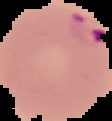

malaria status = parasitized
preparation = thin blood film
image size = 112×121 pixels
image type = segmented cell region on a black background